Classify this cell by malaria status.
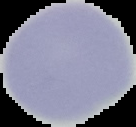

It is uninfected.

image type = segmented cell region on a black background
image size = 136×127 pixels
preparation = thin blood smear